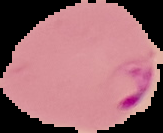

result = malaria parasites identified
preparation = thin blood smear
image type = segmented cell region with the area outside set to black
image size = 163×133 pixels